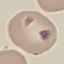
{
  "malaria_status": "uninfected",
  "capture": "smartphone through the microscope eyepiece",
  "stain": "Giemsa",
  "image_type": "cell patch, automatically extracted from a larger field of view and resized to 64 × 64 pixels",
  "preparation": "thin blood film"
}